Assess the morphology of the red blood cells.
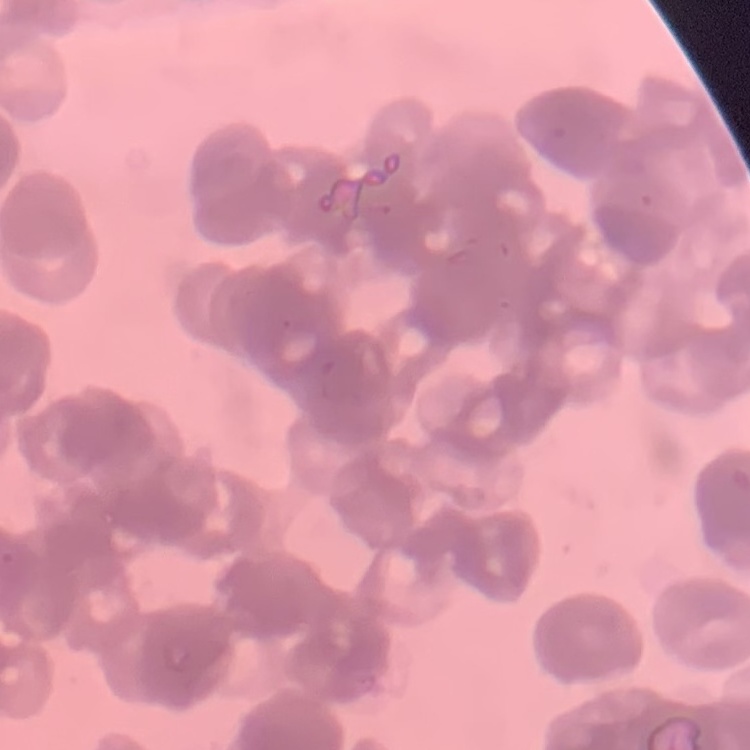
Rouleaux formation.

image type = square crop of a larger photomicrograph
stain = Field's or Giemsa
preparation = thin peripheral smear